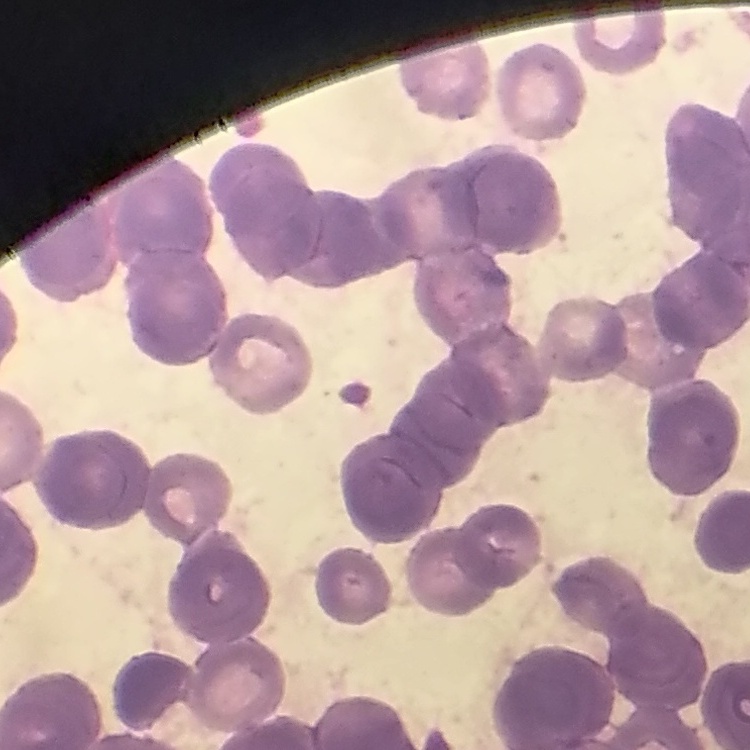

The erythrocytes show rouleaux formation. Thin peripheral smear. Field's or Giemsa stain. Square crop of a larger photomicrograph.